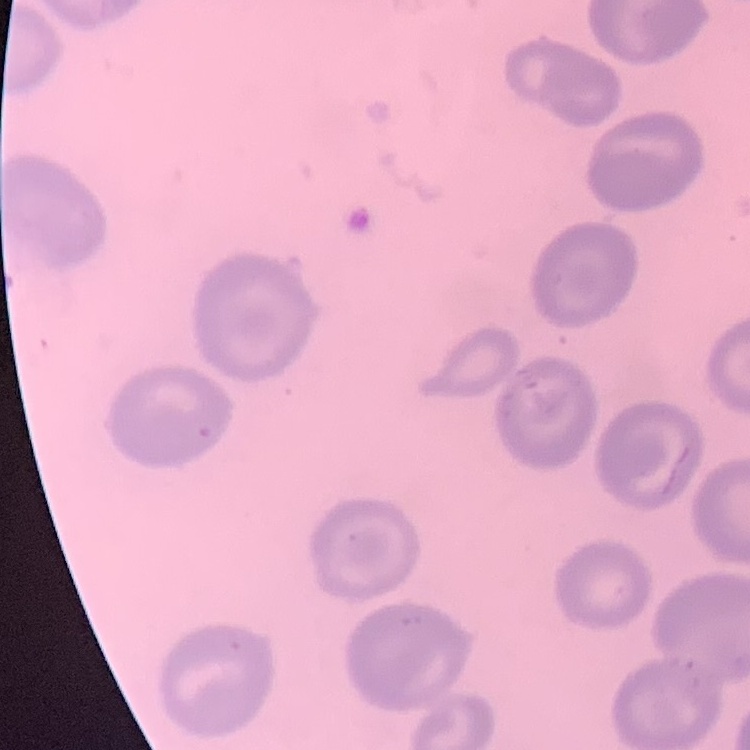

red blood cell morphology = no rouleaux formation
image type = one tile cut from a larger photomicrograph
preparation = thin blood smear
stain = Field's or Giemsa